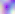
Toxoplasma gondii is seen. 400x magnification. Micrograph.